Report the malaria status of this cell.
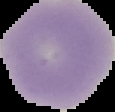

Uninfected.

Summary:
  - Image size: 115×112 pixels
  - Preparation: thin blood film
  - Image type: segmented cell region with the area outside set to black